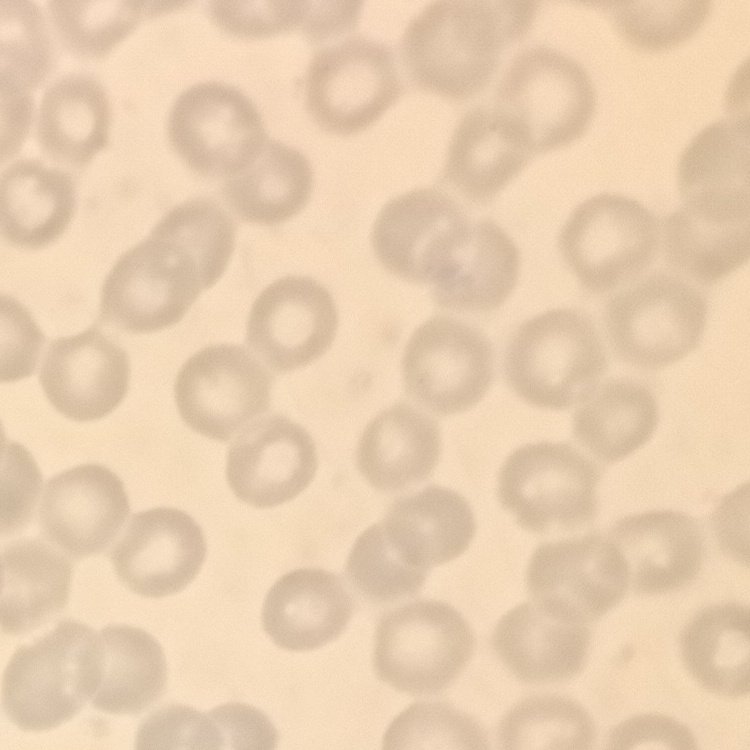
Summary:
  - Red blood cell morphology: no rouleaux formation
  - Preparation: thin blood smear
  - Stain: Field's or Giemsa
  - Image type: square crop of a larger photomicrograph